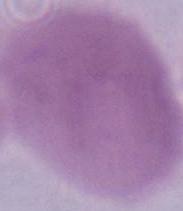
modality = photomicrograph
magnification = 1000x
identification = erythrocyte